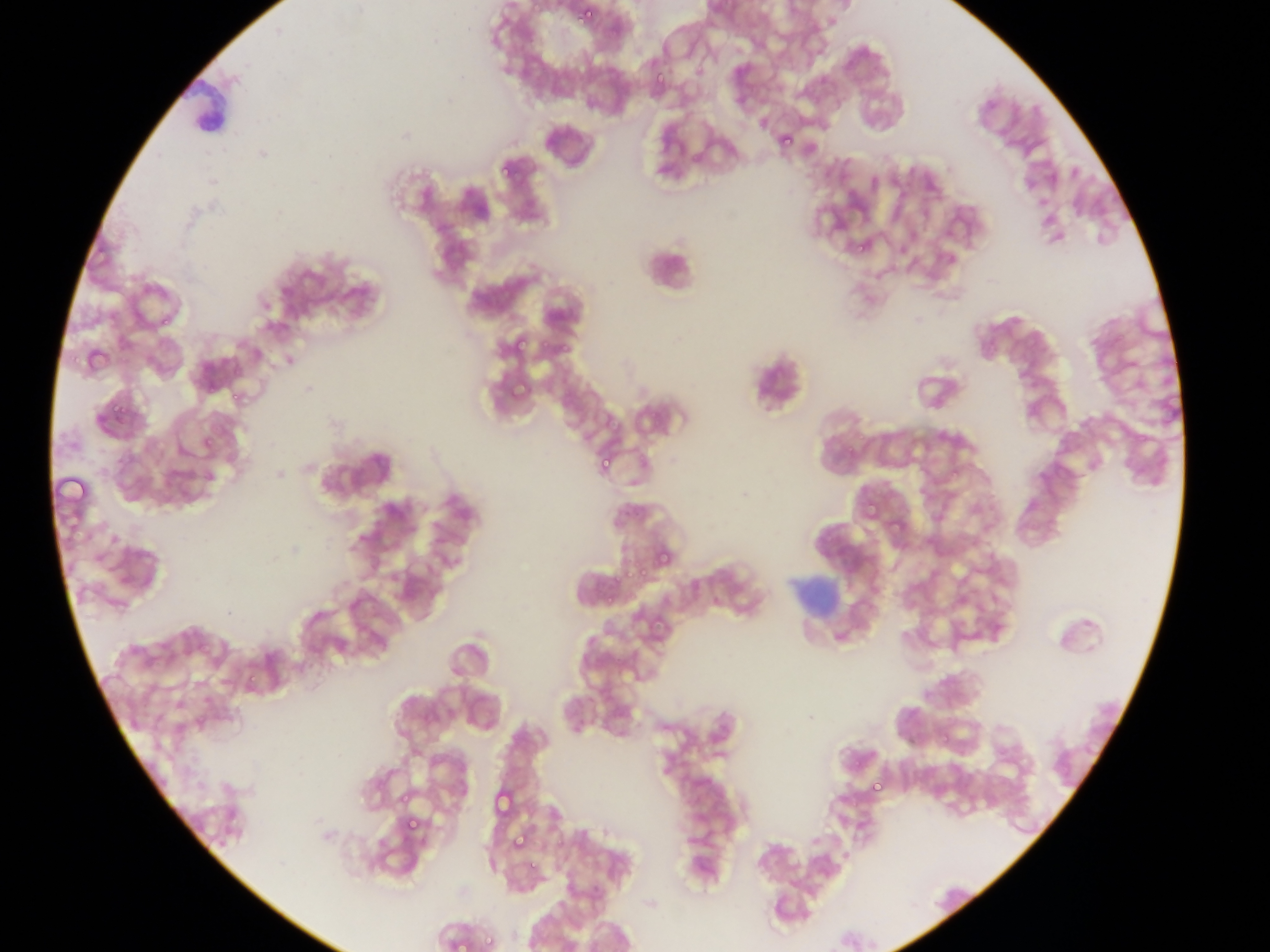 Approximate bounding boxes as (left, top, right, bottom) in pixels. Malaria parasite locations: (580, 5, 597, 24), (652, 58, 670, 92), (778, 117, 804, 147), (498, 169, 508, 176), (852, 234, 869, 259), (541, 331, 551, 353), (515, 334, 531, 355), (555, 338, 573, 355), (511, 370, 532, 403), (229, 386, 240, 406), (106, 391, 130, 420), (201, 435, 216, 451), (1134, 435, 1146, 446), (599, 454, 613, 471), (948, 464, 969, 485), (861, 499, 872, 526), (889, 514, 905, 532), (652, 547, 672, 566), (621, 560, 639, 586), (637, 562, 655, 575), (604, 596, 614, 610), (940, 726, 950, 744), (871, 775, 884, 797), (494, 779, 510, 820), (396, 790, 414, 812), (406, 820, 416, 831), (510, 832, 527, 852), (527, 852, 542, 871), (476, 930, 499, 948) | approximate (x, y) pixel centers of objects too small to bound: (162, 321). Leukocyte locations: (638, 231, 706, 300). Image is 1270×952 pixels. Thin blood film. Photographed through a microscope with a mobile-phone camera. Single field of view. Sample from Ghana.